Assess this cell for malaria.
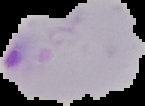
Parasitized.

preparation: thin blood smear
image_size: 145×106 pixels
image_type: cell region segmented out of the field of view; surrounding area masked to black